Assess this cell for malaria.
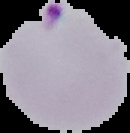

Parasitized.

Summary:
  - Preparation: thin blood film
  - Image type: segmented cell region with the area outside set to black
  - Image size: 130×133 pixels